Identify the cell.
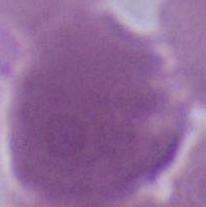
An erythrocyte.

Summary:
  - Magnification: 1000x
  - Modality: photomicrograph